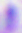
identification = Toxoplasma gondii
modality = micrograph
magnification = 400x